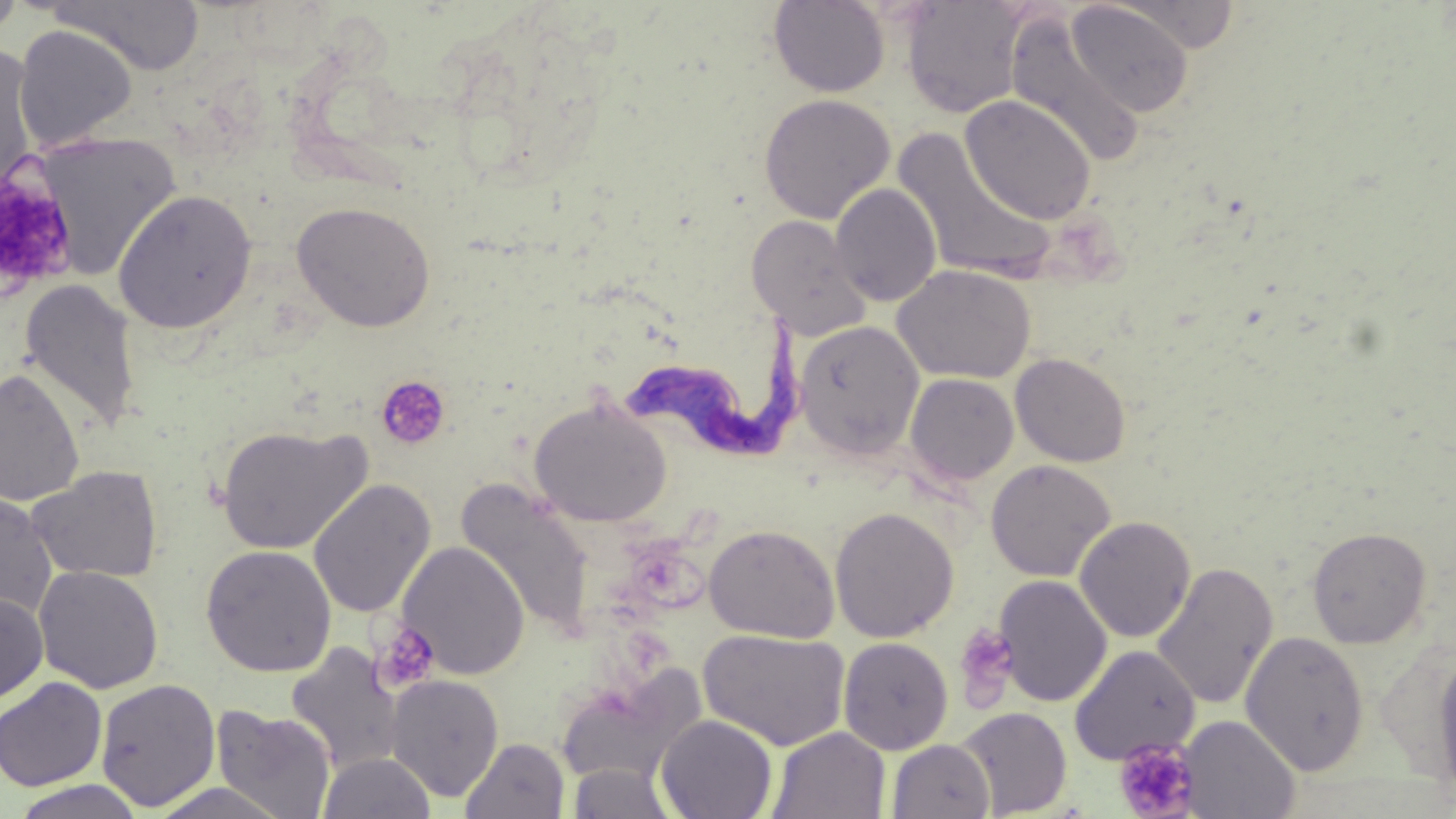

Summary:
  - Coordinate format: approximate bounding boxes as [x1, y1, x2, y2] in pixels
  - Platelet locations: [0, 165, 80, 300], [376, 376, 450, 451], [371, 622, 440, 693], [952, 623, 1021, 710], [1113, 739, 1198, 818]
  - Trypanosoma brucei locations: [617, 308, 805, 460]
  - Uninfected red blood cell locations: [0, 0, 25, 44], [48, 0, 205, 75], [768, 0, 890, 97], [901, 0, 1032, 118], [1067, 1, 1194, 117], [1116, 2, 1240, 54], [1004, 14, 1145, 168], [13, 24, 139, 151], [0, 45, 41, 192], [758, 94, 896, 224], [960, 94, 1097, 225], [891, 128, 1058, 284], [30, 132, 182, 281], [830, 183, 942, 307], [113, 189, 257, 334], [291, 201, 437, 332], [746, 215, 871, 340], [893, 265, 1035, 384], [19, 279, 142, 435], [794, 320, 925, 460], [1011, 353, 1131, 468], [0, 369, 85, 507], [905, 373, 1019, 486], [529, 398, 673, 528], [216, 423, 372, 555], [985, 460, 1116, 582], [28, 465, 163, 584], [308, 479, 435, 619], [456, 479, 594, 639], [0, 491, 58, 622], [830, 506, 960, 643], [1074, 516, 1196, 643], [703, 523, 840, 642], [1307, 526, 1432, 648], [397, 541, 531, 679], [201, 544, 337, 677], [1152, 562, 1279, 711], [34, 565, 163, 693], [993, 575, 1112, 707], [0, 593, 49, 705], [698, 628, 851, 751], [1240, 630, 1370, 776], [838, 637, 953, 754], [285, 643, 405, 775], [1069, 645, 1200, 765], [1433, 648, 1456, 806], [553, 664, 705, 787], [385, 674, 505, 801], [0, 677, 107, 792], [95, 677, 222, 811], [212, 705, 336, 818], [956, 707, 1072, 818], [655, 714, 778, 819], [1180, 715, 1300, 818], [768, 727, 890, 819], [460, 737, 569, 818], [887, 739, 996, 819], [318, 752, 436, 819], [567, 763, 677, 818], [9, 779, 147, 818], [147, 782, 295, 819]
  - Slide-level diagnosis: Trypanosoma brucei
  - Field of view: single
  - Modality: optical microscopy
  - Preparation: thin blood smear
  - Image size: 1456×819 pixels
  - Magnification: 1000x
  - Stain: May-Grünwald-Giemsa